Describe the morphology of the erythrocytes.
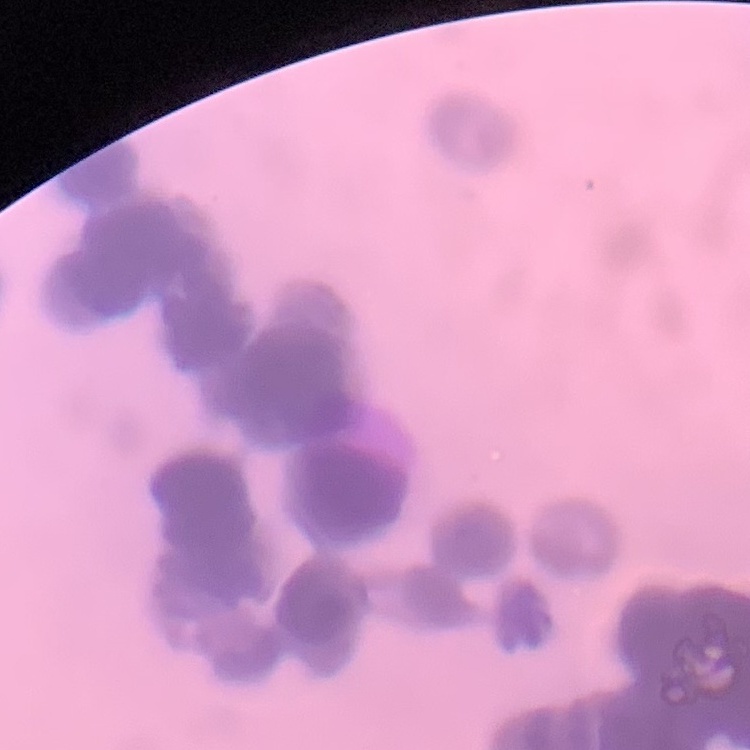

Rouleaux formation.

{
  "stain": "Field's or Giemsa",
  "image_type": "square crop of a larger photomicrograph",
  "preparation": "thin blood smear"
}